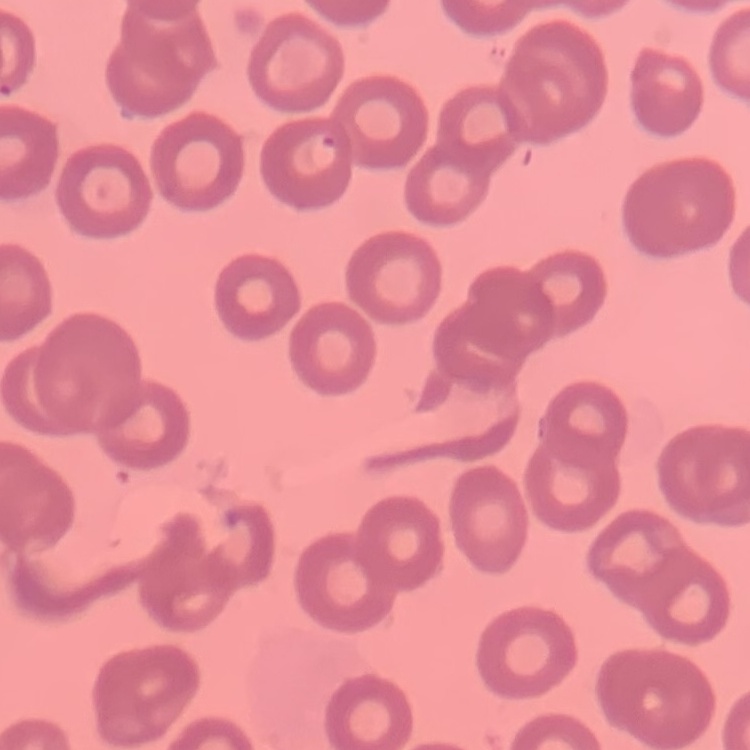

Summary:
  - Red blood cell morphology: no rouleaux formation
  - Preparation: thin blood film
  - Image type: square crop of a larger photomicrograph
  - Stain: Field's or Giemsa